Name the parasite shown.
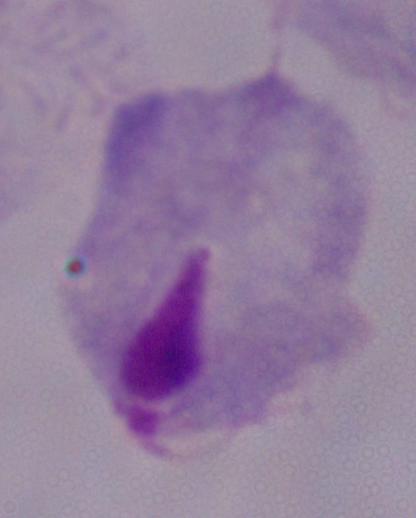
This is a trichomonad.

{
  "modality": "photomicrograph",
  "magnification": "1000x"
}